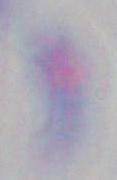 Captured at 1000x magnification. Micrograph. Toxoplasma gondii is shown.